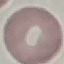
Summary:
  - Result: no malaria parasites detected
  - Stain: Giemsa
  - Image type: automatically extracted cell patch, resized to 64 × 64 pixels
  - Preparation: thin blood film
  - Capture: smartphone through the microscope eyepiece